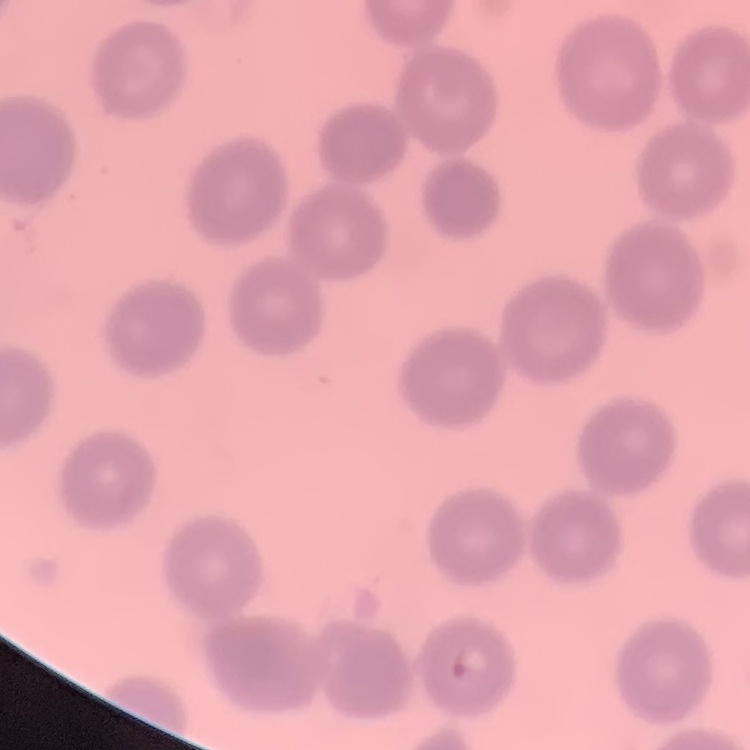

Summary:
  - Erythrocyte morphology: no rouleaux formation
  - Preparation: thin peripheral smear
  - Stain: Field's or Giemsa
  - Image type: one tile cut from a larger photomicrograph